Identify the blood parasite species.
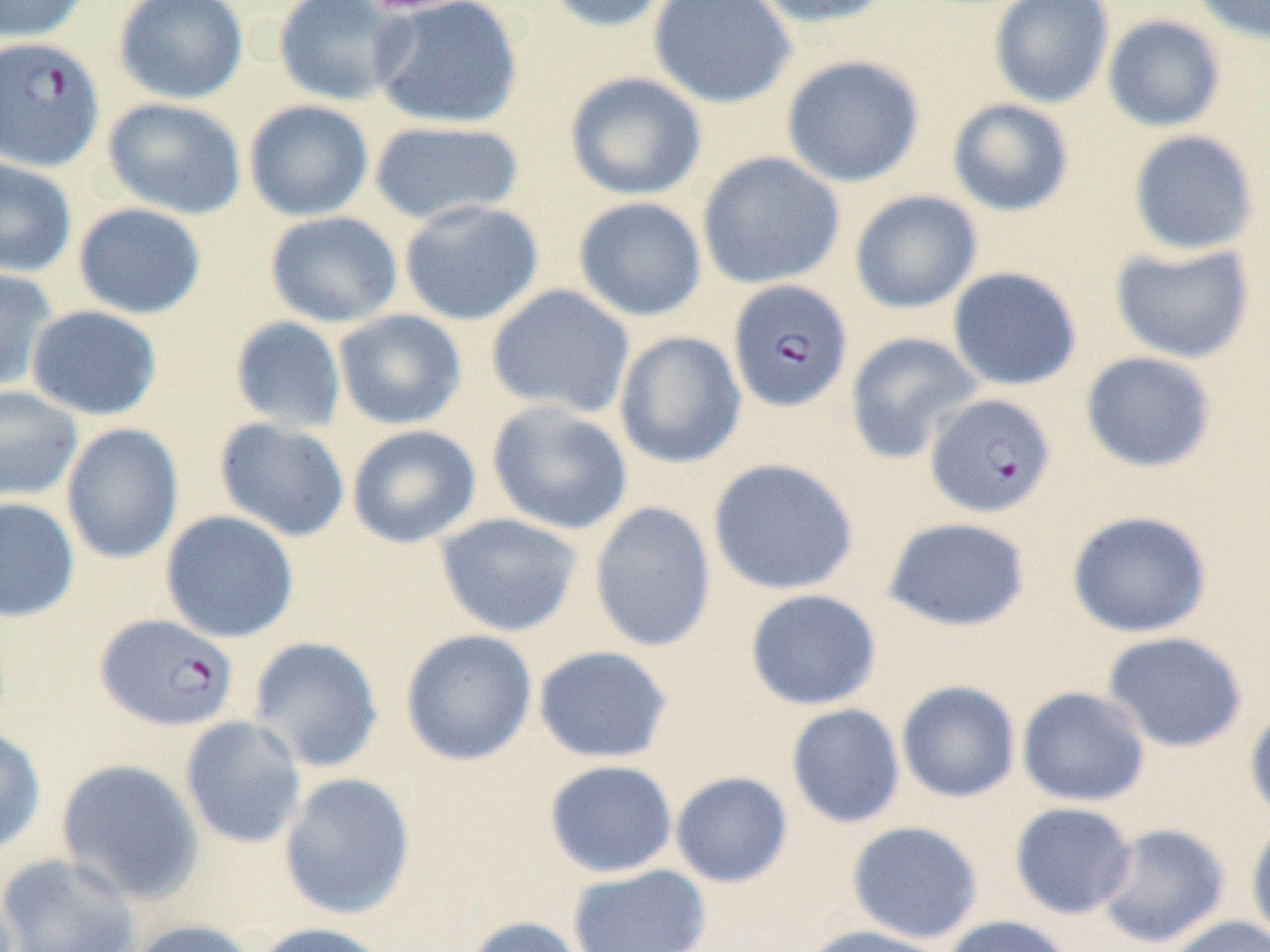
Plasmodium falciparum.

Summary:
  - Coordinate format: approximate bounding boxes as named x1/y1/x2/y2 corners in pixels
  - Plasmodium falciparum-infected red blood cell locations: (x1=0, y1=36, x2=105, y2=172), (x1=728, y1=279, x2=853, y2=413), (x1=924, y1=393, x2=1056, y2=518), (x1=95, y1=613, x2=239, y2=732)
  - Uninfected red blood cell locations: (x1=0, y1=0, x2=91, y2=43), (x1=113, y1=0, x2=248, y2=105), (x1=272, y1=0, x2=413, y2=106), (x1=371, y1=0, x2=524, y2=130), (x1=542, y1=0, x2=674, y2=33), (x1=648, y1=0, x2=796, y2=109), (x1=746, y1=0, x2=897, y2=29), (x1=989, y1=0, x2=1114, y2=108), (x1=1188, y1=0, x2=1270, y2=44), (x1=1102, y1=15, x2=1226, y2=133), (x1=781, y1=54, x2=925, y2=188), (x1=564, y1=71, x2=707, y2=200), (x1=102, y1=97, x2=247, y2=220), (x1=947, y1=98, x2=1074, y2=217), (x1=244, y1=99, x2=374, y2=221), (x1=368, y1=119, x2=525, y2=226), (x1=1127, y1=129, x2=1260, y2=257), (x1=697, y1=151, x2=845, y2=289), (x1=0, y1=157, x2=77, y2=278), (x1=849, y1=190, x2=982, y2=314), (x1=572, y1=196, x2=707, y2=321), (x1=399, y1=198, x2=545, y2=326), (x1=72, y1=202, x2=206, y2=319), (x1=264, y1=210, x2=403, y2=328), (x1=1109, y1=241, x2=1255, y2=364), (x1=0, y1=266, x2=58, y2=394), (x1=947, y1=266, x2=1082, y2=391), (x1=486, y1=284, x2=635, y2=418), (x1=25, y1=305, x2=162, y2=420), (x1=333, y1=309, x2=467, y2=430), (x1=229, y1=316, x2=347, y2=433), (x1=614, y1=330, x2=746, y2=470), (x1=844, y1=331, x2=984, y2=465), (x1=1080, y1=351, x2=1217, y2=473), (x1=0, y1=386, x2=83, y2=503), (x1=487, y1=400, x2=633, y2=536), (x1=213, y1=418, x2=350, y2=542), (x1=60, y1=423, x2=184, y2=565), (x1=346, y1=424, x2=481, y2=548), (x1=708, y1=458, x2=859, y2=596), (x1=0, y1=496, x2=80, y2=623), (x1=589, y1=501, x2=717, y2=652), (x1=160, y1=510, x2=299, y2=643), (x1=1066, y1=510, x2=1212, y2=638), (x1=434, y1=512, x2=584, y2=637), (x1=882, y1=517, x2=1031, y2=632), (x1=744, y1=588, x2=881, y2=711), (x1=400, y1=629, x2=538, y2=766), (x1=1101, y1=631, x2=1248, y2=753), (x1=246, y1=635, x2=384, y2=773), (x1=532, y1=645, x2=674, y2=763), (x1=895, y1=680, x2=1021, y2=803), (x1=1016, y1=686, x2=1150, y2=807), (x1=1244, y1=702, x2=1270, y2=824), (x1=786, y1=703, x2=905, y2=828), (x1=179, y1=715, x2=307, y2=849), (x1=0, y1=727, x2=46, y2=856), (x1=56, y1=758, x2=204, y2=906), (x1=544, y1=759, x2=678, y2=878), (x1=670, y1=771, x2=793, y2=888), (x1=278, y1=772, x2=416, y2=920), (x1=1009, y1=801, x2=1137, y2=919), (x1=1245, y1=818, x2=1270, y2=947), (x1=847, y1=820, x2=983, y2=944), (x1=1095, y1=823, x2=1230, y2=949), (x1=0, y1=852, x2=140, y2=952), (x1=567, y1=863, x2=711, y2=952), (x1=462, y1=915, x2=587, y2=952), (x1=939, y1=915, x2=1078, y2=952), (x1=1166, y1=915, x2=1270, y2=952), (x1=127, y1=919, x2=260, y2=952), (x1=252, y1=921, x2=395, y2=952), (x1=801, y1=925, x2=951, y2=952)
  - Image size: 1270×952 pixels
  - Preparation: thin blood film
  - Modality: light microscopy
  - Magnification: 1000x
  - Stain: May-Grünwald-Giemsa
  - Field of view: one of a larger specimen